Point out Plasmodium parasites and leukocytes.
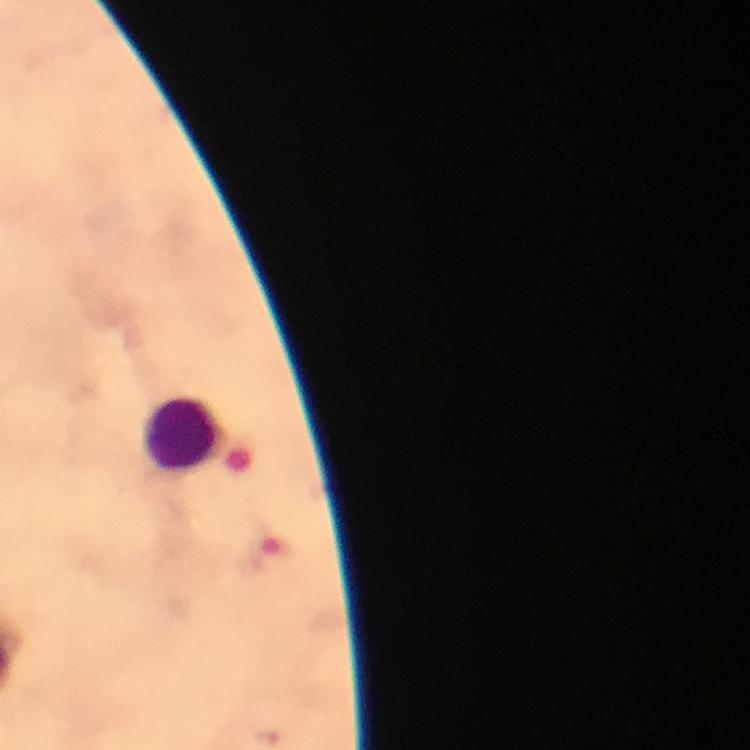
No Plasmodium parasites detected.
Approximate centers as [x, y] in pixels.
Leukocytes: [182, 435].

Giemsa stain. 100x magnification. Thick blood film. From a malaria diagnostic workup. Photographed through the microscope with a smartphone camera. Immersion oil applied. Image is 750×750 pixels. A crop from one field of view.